Name the parasite shown.
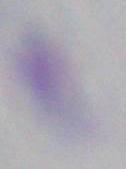

This is Toxoplasma gondii.

modality = photomicrograph
magnification = 1000x